Locate every Plasmodium parasite.
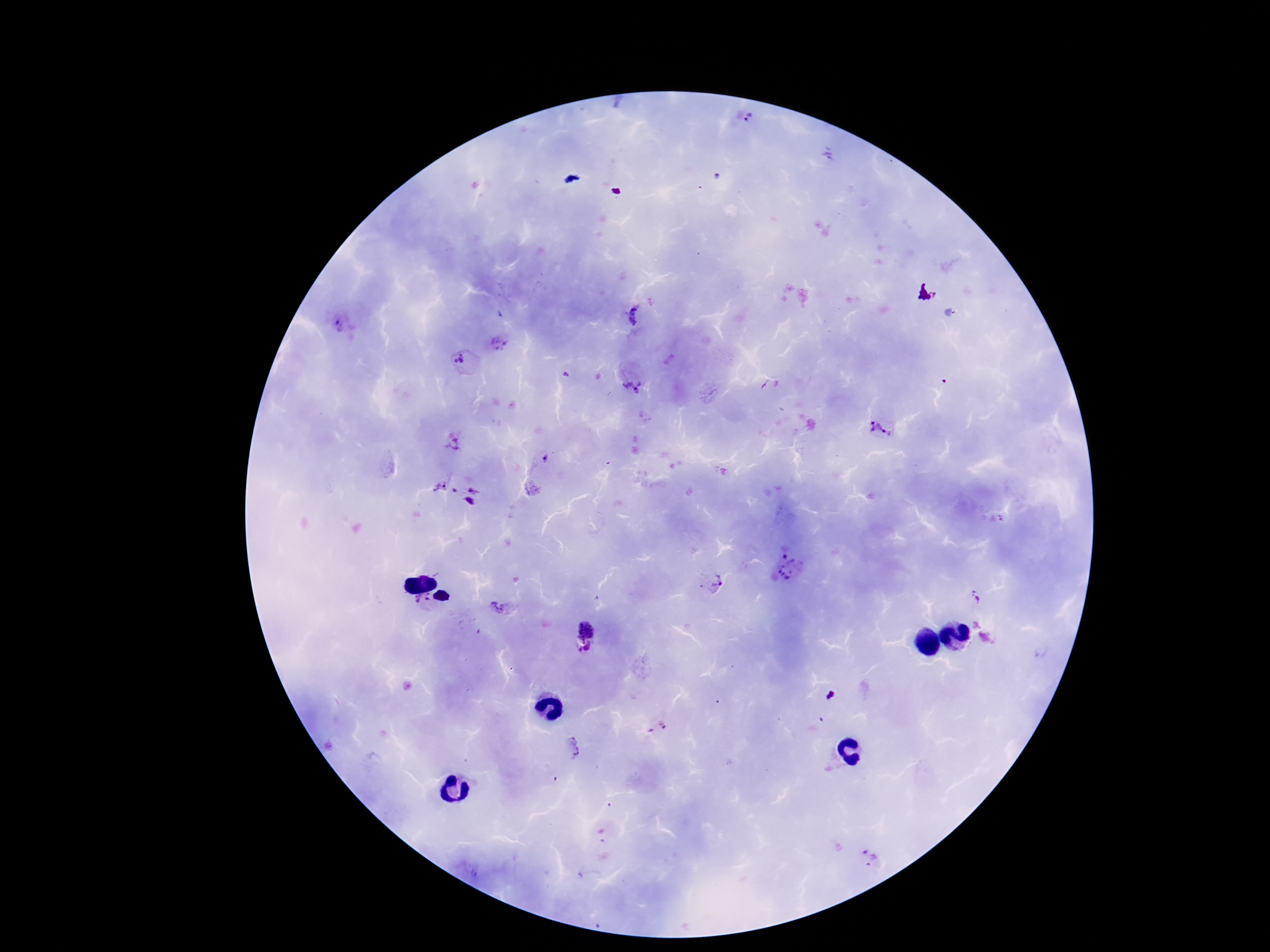

Approximate centers as {x, y} in pixels.
Plasmodium parasites: {746, 118}, {338, 326}, {498, 344}, {459, 358}, {566, 374}, {632, 387}, {881, 430}, {455, 443}, {438, 482}, {475, 488}, {455, 491}, {469, 502}, {791, 569}, {716, 585}, {975, 596}, {423, 602}, {498, 606}, {977, 624}, {586, 628}, {986, 638}, {589, 647}, {580, 650}, {573, 747}, {868, 858}.

preparation = thick peripheral-blood smear
patient malaria status = positive
magnification = 100x
image size = 1270×952 pixels
capture = smartphone camera through the microscope eyepiece
field of view = one from this slide
stain = Giemsa